Locate platelets.
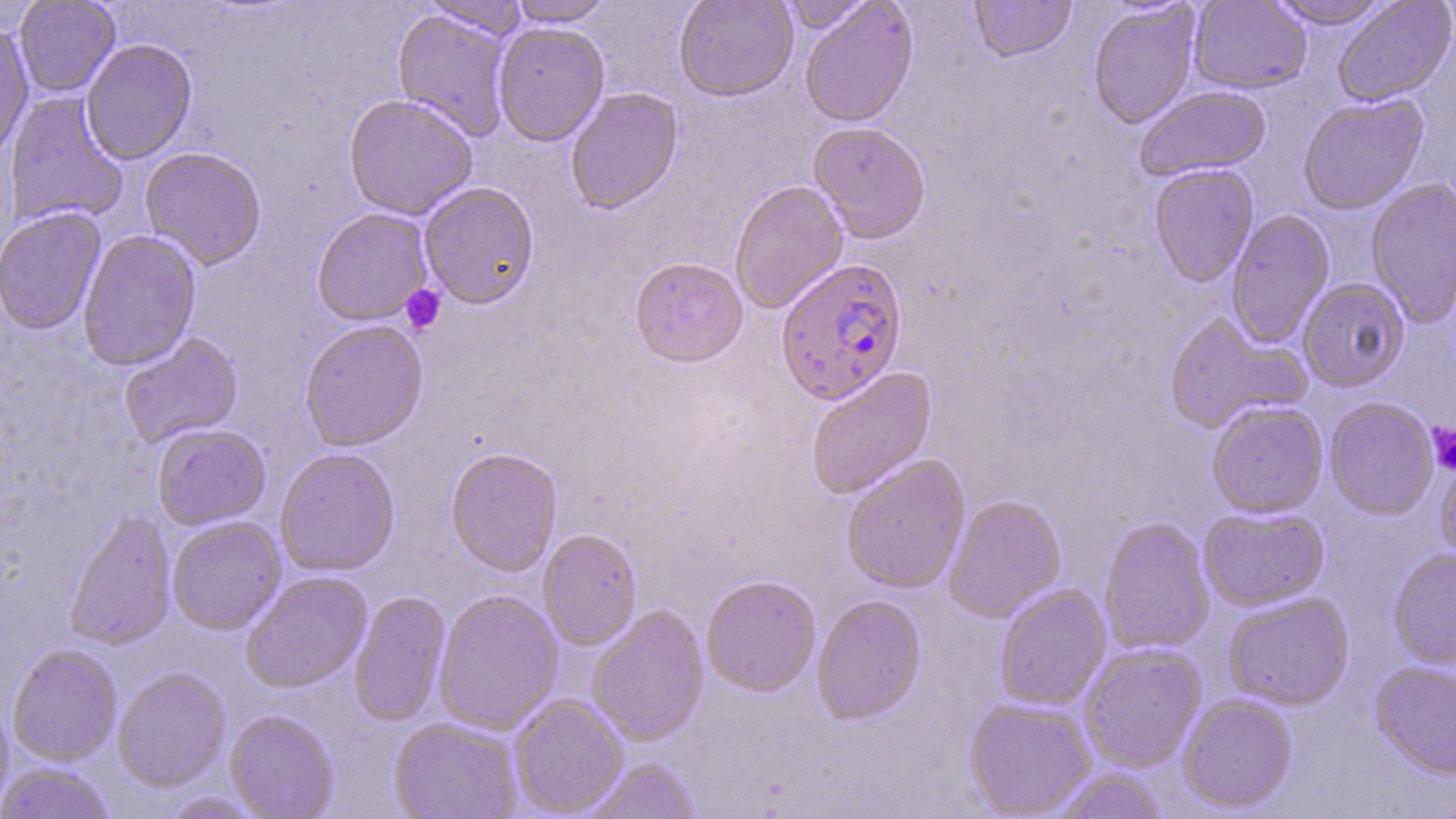

Approximate bounding boxes as (x1, y1, x2, y2) in pixels.
Platelets: (400, 284, 446, 335), (1427, 423, 1456, 474).

Plasmodium falciparum-infected red blood cell locations: (775, 258, 909, 405). Uninfected red blood cell locations: (14, 0, 120, 97), (418, 0, 530, 42), (508, 0, 617, 26), (673, 0, 798, 102), (777, 0, 876, 34), (970, 0, 1076, 64), (1188, 0, 1311, 95), (1265, 0, 1396, 30), (1332, 0, 1456, 109), (799, 1, 919, 128), (1088, 2, 1201, 130), (392, 8, 514, 142), (493, 22, 609, 146), (0, 23, 34, 161), (80, 39, 197, 165), (1134, 86, 1271, 183), (566, 87, 683, 215), (3, 93, 128, 227), (343, 93, 478, 220), (1298, 96, 1428, 216), (808, 123, 931, 244), (140, 147, 267, 270), (1149, 164, 1259, 288), (1366, 178, 1456, 327), (730, 180, 849, 314), (418, 182, 540, 309), (1, 207, 106, 336), (312, 208, 433, 326), (1226, 210, 1335, 347), (77, 230, 201, 371), (629, 257, 748, 368), (1298, 278, 1410, 393), (1164, 313, 1309, 434), (299, 320, 428, 451), (119, 333, 243, 448), (805, 367, 938, 500), (1324, 398, 1438, 519), (1206, 401, 1328, 518), (153, 424, 271, 530), (445, 447, 563, 577), (275, 448, 400, 577), (1434, 453, 1456, 567), (841, 455, 970, 593), (943, 494, 1066, 622), (1199, 507, 1329, 611), (63, 510, 176, 651), (167, 516, 286, 635), (1099, 516, 1215, 655), (538, 529, 641, 650), (1388, 549, 1456, 670), (240, 571, 372, 694), (701, 575, 821, 696), (995, 584, 1112, 711), (433, 590, 563, 735), (349, 591, 451, 727), (1223, 591, 1355, 710), (812, 596, 926, 724), (587, 604, 709, 746), (1079, 643, 1207, 772), (7, 644, 122, 766), (1370, 662, 1456, 780), (113, 669, 230, 792), (1177, 693, 1297, 813), (0, 694, 14, 814), (509, 695, 628, 816), (964, 698, 1097, 817), (225, 711, 340, 819), (389, 717, 522, 819), (582, 758, 702, 819), (0, 763, 116, 819), (1050, 767, 1169, 818), (158, 791, 266, 818). Slide-level diagnosis: Plasmodium falciparum. Single field of view. Thin blood film. May-Grünwald-Giemsa stain. Light microscopy. Captured at 1000x magnification. Image is 1456×819 pixels.